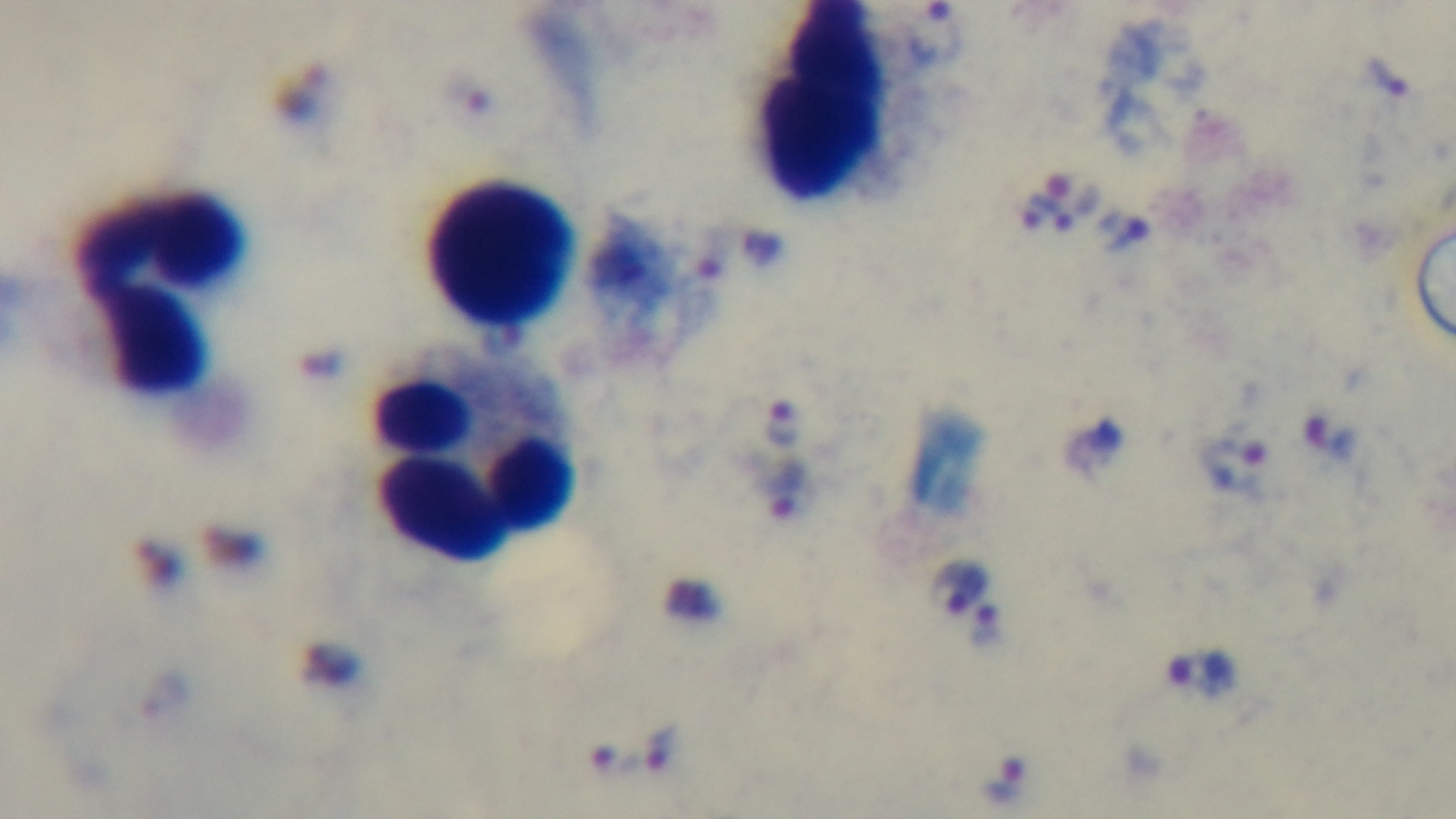

modality = light microscopy
objective = 100x oil immersion
preparation = thick smear
capture = mounted 4K digital camera
malaria status = infected
stain = Giemsa
field of view = single